Outline platelets.
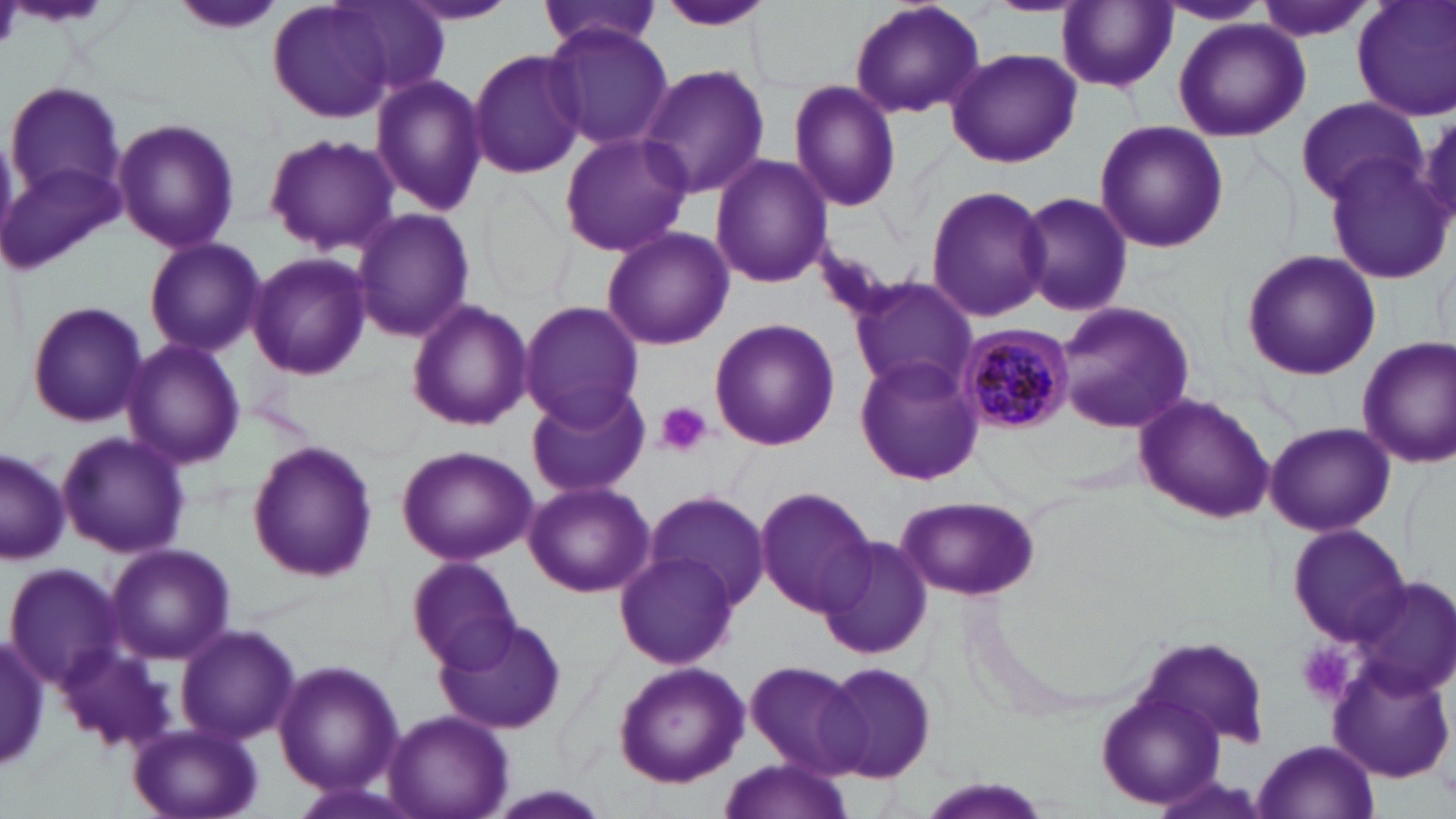
Approximate bounding boxes as named x1/y1/x2/y2 corners in pixels.
Platelets: (x1=653, y1=401, x2=712, y2=458), (x1=1295, y1=641, x2=1359, y2=706).

Summary:
  - Plasmodium malariae-infected red blood cell locations: (x1=956, y1=323, x2=1072, y2=434)
  - Uninfected red blood cell locations: (x1=175, y1=0, x2=284, y2=37), (x1=267, y1=0, x2=420, y2=124), (x1=1255, y1=0, x2=1378, y2=41), (x1=1353, y1=0, x2=1456, y2=123), (x1=400, y1=1, x2=519, y2=26), (x1=847, y1=1, x2=986, y2=120), (x1=1156, y1=1, x2=1270, y2=26), (x1=331, y1=2, x2=451, y2=102), (x1=538, y1=2, x2=663, y2=54), (x1=654, y1=2, x2=779, y2=32), (x1=1057, y1=2, x2=1178, y2=93), (x1=1172, y1=18, x2=1311, y2=141), (x1=543, y1=21, x2=672, y2=153), (x1=469, y1=48, x2=589, y2=179), (x1=945, y1=48, x2=1080, y2=168), (x1=637, y1=62, x2=771, y2=198), (x1=370, y1=74, x2=487, y2=216), (x1=789, y1=79, x2=903, y2=214), (x1=4, y1=80, x2=123, y2=201), (x1=1296, y1=98, x2=1426, y2=206), (x1=112, y1=118, x2=241, y2=253), (x1=1092, y1=120, x2=1228, y2=253), (x1=557, y1=130, x2=693, y2=258), (x1=262, y1=133, x2=400, y2=256), (x1=711, y1=155, x2=834, y2=289), (x1=568, y1=156, x2=713, y2=327), (x1=2, y1=159, x2=124, y2=275), (x1=1326, y1=161, x2=1454, y2=284), (x1=926, y1=186, x2=1054, y2=323), (x1=1017, y1=190, x2=1135, y2=319), (x1=352, y1=209, x2=474, y2=340), (x1=601, y1=226, x2=734, y2=351), (x1=145, y1=238, x2=265, y2=356), (x1=1241, y1=248, x2=1382, y2=380), (x1=248, y1=251, x2=372, y2=380), (x1=846, y1=276, x2=978, y2=398), (x1=25, y1=299, x2=150, y2=430), (x1=406, y1=300, x2=533, y2=432), (x1=519, y1=301, x2=646, y2=428), (x1=1053, y1=302, x2=1195, y2=434), (x1=708, y1=317, x2=839, y2=451), (x1=1357, y1=335, x2=1456, y2=466), (x1=121, y1=338, x2=246, y2=470), (x1=854, y1=355, x2=985, y2=486), (x1=524, y1=384, x2=651, y2=500), (x1=1132, y1=391, x2=1277, y2=525), (x1=1264, y1=422, x2=1394, y2=538), (x1=55, y1=429, x2=191, y2=560), (x1=246, y1=442, x2=378, y2=583), (x1=396, y1=445, x2=537, y2=565), (x1=0, y1=449, x2=71, y2=567), (x1=523, y1=480, x2=655, y2=597), (x1=754, y1=484, x2=879, y2=616), (x1=646, y1=490, x2=770, y2=610), (x1=896, y1=493, x2=1039, y2=600), (x1=1284, y1=523, x2=1413, y2=647), (x1=819, y1=534, x2=935, y2=659), (x1=106, y1=542, x2=235, y2=665), (x1=614, y1=551, x2=738, y2=669), (x1=406, y1=557, x2=520, y2=671), (x1=5, y1=563, x2=122, y2=687), (x1=1344, y1=578, x2=1456, y2=702), (x1=433, y1=613, x2=570, y2=737), (x1=175, y1=624, x2=300, y2=746), (x1=1, y1=630, x2=49, y2=773), (x1=56, y1=640, x2=179, y2=754), (x1=743, y1=659, x2=868, y2=776), (x1=1328, y1=659, x2=1455, y2=785), (x1=274, y1=660, x2=402, y2=796), (x1=612, y1=661, x2=750, y2=787), (x1=822, y1=661, x2=938, y2=784), (x1=1096, y1=687, x2=1230, y2=808), (x1=385, y1=709, x2=513, y2=819), (x1=128, y1=723, x2=263, y2=819), (x1=1252, y1=739, x2=1379, y2=818), (x1=713, y1=760, x2=853, y2=819), (x1=480, y1=786, x2=617, y2=819)
  - Slide-level diagnosis: Plasmodium malariae
  - Magnification: 1000x
  - Field of view: single
  - Preparation: thin blood film
  - Image size: 1456×819 pixels
  - Modality: optical microscopy
  - Stain: May-Grünwald-Giemsa